Give a bounding box for every malaria parasite, every leukocyte, and every artifact (stain precipitate or debris).
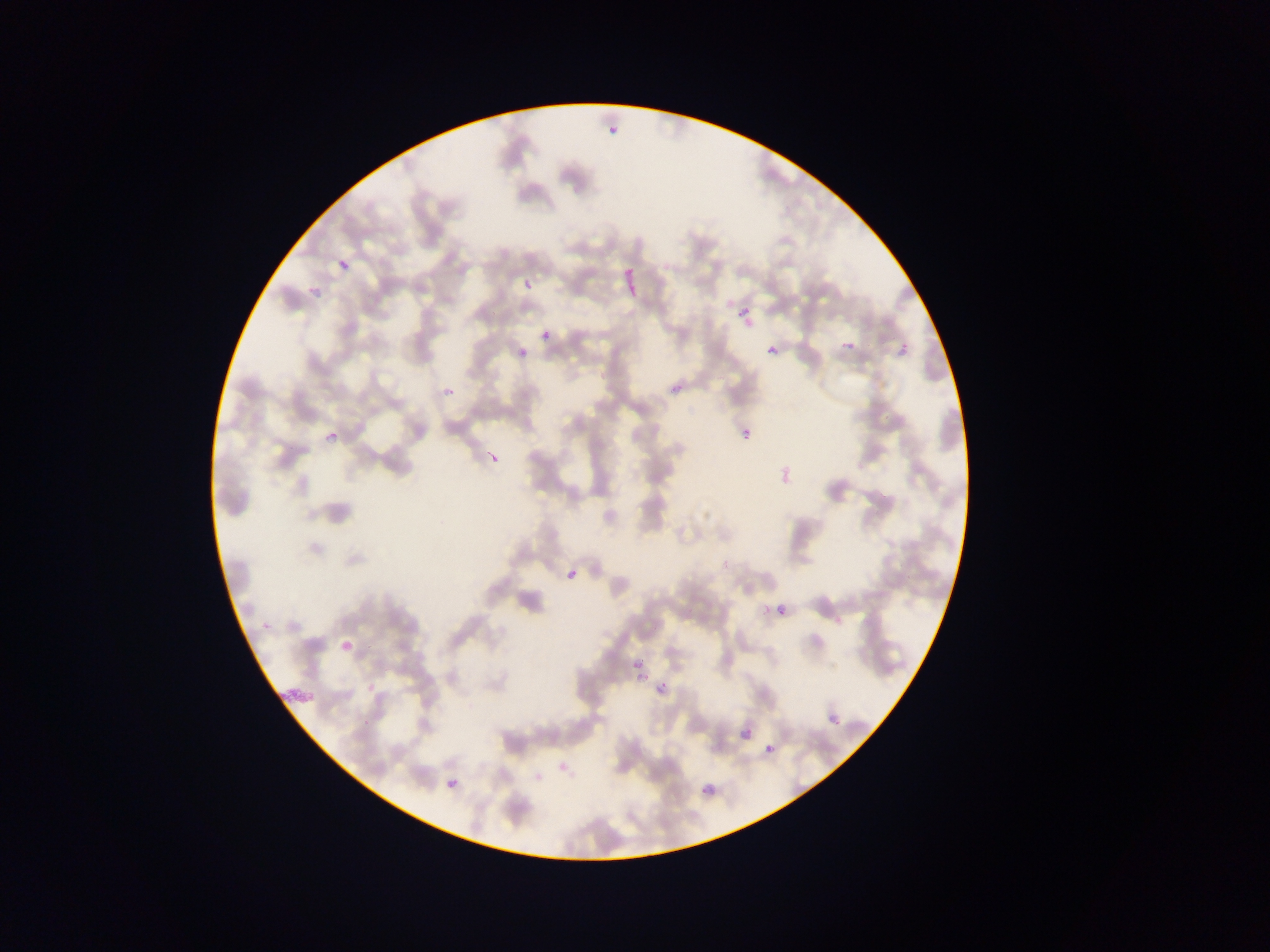
Approximate bounding boxes as (left, top, right, bottom) in pixels.
Malaria parasites: (607, 109, 625, 136), (338, 244, 358, 268), (524, 279, 532, 288), (307, 280, 329, 297), (724, 299, 733, 308), (738, 305, 751, 320), (541, 331, 550, 341), (896, 334, 915, 356), (840, 341, 853, 355), (767, 345, 778, 355), (516, 347, 534, 369), (440, 379, 457, 402), (742, 429, 751, 439), (326, 431, 340, 443), (568, 570, 577, 578), (777, 604, 787, 614), (762, 605, 770, 614), (636, 666, 655, 680), (655, 672, 680, 691), (829, 713, 841, 725), (741, 728, 753, 740), (765, 744, 774, 754), (558, 761, 568, 771), (446, 778, 458, 789), (701, 787, 709, 794).
No leukocytes observed.

One field of view. Image is 1270×952 pixels. Photographed through a microscope with a mobile-phone camera. Thin blood smear. Collected in Ghana.